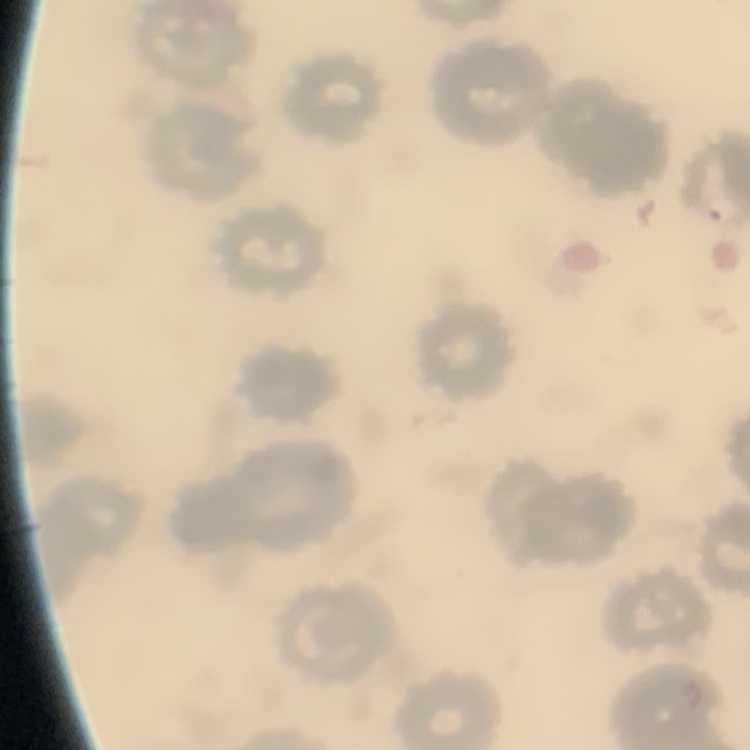
Summary:
  - Erythrocyte morphology: no rouleaux formation
  - Image type: square crop of a larger photomicrograph
  - Preparation: thin blood smear
  - Stain: Field's or Giemsa